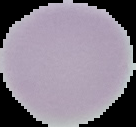
Image is 136×127 pixels. Malaria status: uninfected. Segmented cell region on a black background. From a thin blood smear.